Outline each Plasmodium vivax-infected red blood cell.
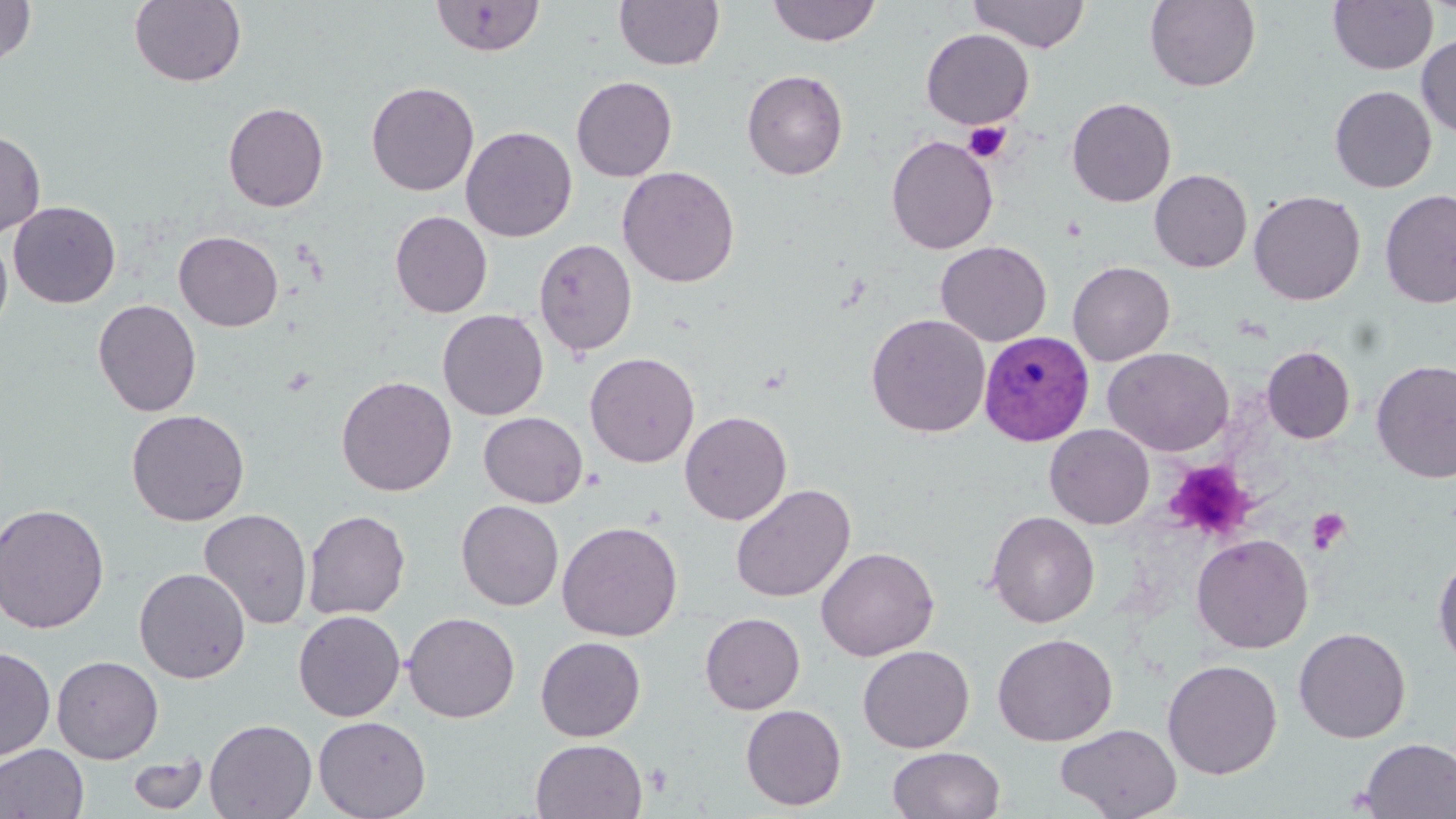
Approximate bounding boxes as named x1/y1/x2/y2 corners in pixels.
Plasmodium vivax-infected red blood cells: (x1=978, y1=330, x2=1095, y2=446).

Uninfected red blood cell locations: (x1=0, y1=0, x2=36, y2=68), (x1=129, y1=0, x2=247, y2=87), (x1=430, y1=0, x2=545, y2=56), (x1=614, y1=0, x2=725, y2=71), (x1=766, y1=0, x2=882, y2=47), (x1=967, y1=0, x2=1090, y2=53), (x1=1145, y1=0, x2=1260, y2=93), (x1=1328, y1=0, x2=1438, y2=74), (x1=920, y1=28, x2=1035, y2=130), (x1=1417, y1=34, x2=1456, y2=138), (x1=741, y1=69, x2=849, y2=180), (x1=571, y1=76, x2=677, y2=182), (x1=366, y1=81, x2=479, y2=196), (x1=1329, y1=85, x2=1437, y2=193), (x1=1066, y1=97, x2=1177, y2=207), (x1=223, y1=102, x2=329, y2=212), (x1=461, y1=126, x2=577, y2=242), (x1=0, y1=129, x2=45, y2=240), (x1=885, y1=134, x2=999, y2=255), (x1=617, y1=166, x2=740, y2=288), (x1=1149, y1=169, x2=1253, y2=272), (x1=1380, y1=188, x2=1456, y2=309), (x1=1248, y1=190, x2=1366, y2=305), (x1=8, y1=201, x2=121, y2=308), (x1=390, y1=210, x2=493, y2=318), (x1=173, y1=231, x2=284, y2=332), (x1=0, y1=233, x2=13, y2=337), (x1=533, y1=238, x2=638, y2=357), (x1=935, y1=240, x2=1052, y2=347), (x1=1067, y1=261, x2=1175, y2=366), (x1=93, y1=298, x2=202, y2=417), (x1=437, y1=309, x2=549, y2=420), (x1=866, y1=313, x2=990, y2=438), (x1=1102, y1=346, x2=1234, y2=457), (x1=1261, y1=346, x2=1356, y2=444), (x1=585, y1=352, x2=700, y2=467), (x1=1371, y1=360, x2=1456, y2=484), (x1=336, y1=375, x2=457, y2=496), (x1=126, y1=409, x2=250, y2=526), (x1=679, y1=410, x2=792, y2=525), (x1=478, y1=412, x2=588, y2=508), (x1=1044, y1=424, x2=1155, y2=530), (x1=730, y1=483, x2=856, y2=603), (x1=456, y1=500, x2=564, y2=611), (x1=0, y1=503, x2=110, y2=634), (x1=198, y1=508, x2=313, y2=629), (x1=303, y1=510, x2=411, y2=620), (x1=986, y1=510, x2=1100, y2=628), (x1=557, y1=521, x2=683, y2=642), (x1=1191, y1=533, x2=1313, y2=654), (x1=816, y1=546, x2=939, y2=661), (x1=1432, y1=551, x2=1456, y2=670), (x1=134, y1=567, x2=251, y2=683), (x1=293, y1=609, x2=405, y2=722), (x1=402, y1=611, x2=520, y2=723), (x1=699, y1=612, x2=805, y2=714), (x1=1293, y1=627, x2=1411, y2=743), (x1=992, y1=632, x2=1117, y2=746), (x1=535, y1=636, x2=646, y2=741), (x1=857, y1=645, x2=975, y2=753), (x1=0, y1=646, x2=56, y2=763), (x1=51, y1=655, x2=164, y2=764), (x1=1162, y1=659, x2=1282, y2=780), (x1=740, y1=704, x2=847, y2=811), (x1=313, y1=715, x2=431, y2=819), (x1=204, y1=718, x2=317, y2=818), (x1=1055, y1=722, x2=1181, y2=819), (x1=1357, y1=737, x2=1456, y2=818), (x1=530, y1=738, x2=648, y2=819), (x1=0, y1=742, x2=89, y2=818), (x1=888, y1=746, x2=1005, y2=819), (x1=127, y1=752, x2=208, y2=814). Platelet locations: (x1=964, y1=122, x2=1010, y2=162), (x1=1166, y1=460, x2=1255, y2=542), (x1=1307, y1=508, x2=1351, y2=554). Slide-level diagnosis: Plasmodium vivax. Light microscopy. Captured at 1000x magnification. Image is 1456×819 pixels. Thin blood film. May-Grünwald-Giemsa-stained preparation. Single field of view.